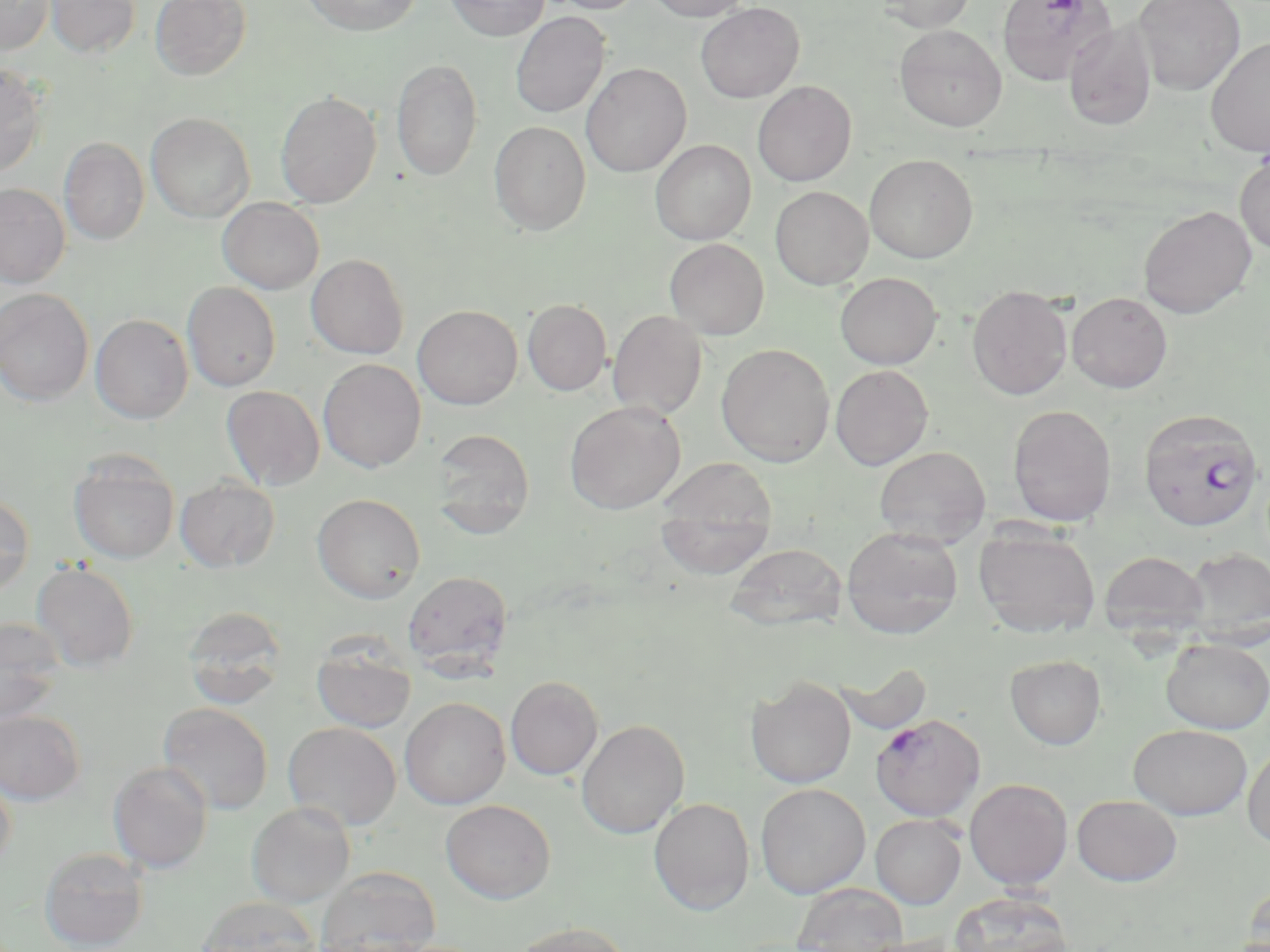

slide-level diagnosis = Plasmodium falciparum
image size = 1270×952 pixels
modality = optical microscopy
stain = May-Grünwald-Giemsa
magnification = 1000x
field of view = one of a larger specimen
preparation = thin blood film
Plasmodium falciparum-infected red blood cell locations = approximate bounding boxes as named x1/y1/x2/y2 corners in pixels: (x1=1138, y1=408, x2=1264, y2=532), (x1=870, y1=713, x2=985, y2=820)
uninfected red blood cell locations = approximate bounding boxes as named x1/y1/x2/y2 corners in pixels: (x1=0, y1=0, x2=54, y2=55), (x1=45, y1=0, x2=141, y2=58), (x1=150, y1=0, x2=252, y2=81), (x1=300, y1=0, x2=422, y2=36), (x1=445, y1=0, x2=548, y2=40), (x1=544, y1=0, x2=646, y2=15), (x1=644, y1=0, x2=754, y2=21), (x1=877, y1=0, x2=976, y2=32), (x1=997, y1=0, x2=1115, y2=86), (x1=1133, y1=0, x2=1246, y2=95), (x1=695, y1=2, x2=804, y2=103), (x1=510, y1=11, x2=610, y2=119), (x1=1064, y1=20, x2=1157, y2=130), (x1=894, y1=25, x2=1007, y2=131), (x1=1205, y1=38, x2=1270, y2=157), (x1=391, y1=58, x2=483, y2=181), (x1=581, y1=63, x2=691, y2=178), (x1=0, y1=64, x2=50, y2=177), (x1=753, y1=81, x2=856, y2=186), (x1=275, y1=91, x2=381, y2=209), (x1=146, y1=112, x2=255, y2=223), (x1=489, y1=121, x2=591, y2=236), (x1=59, y1=138, x2=149, y2=245), (x1=650, y1=139, x2=756, y2=245), (x1=864, y1=154, x2=978, y2=263), (x1=1234, y1=156, x2=1270, y2=255), (x1=0, y1=183, x2=70, y2=287), (x1=770, y1=186, x2=873, y2=289), (x1=217, y1=197, x2=324, y2=294), (x1=1138, y1=205, x2=1257, y2=318), (x1=664, y1=238, x2=769, y2=340), (x1=306, y1=253, x2=409, y2=359), (x1=835, y1=273, x2=942, y2=369), (x1=182, y1=281, x2=281, y2=392), (x1=967, y1=285, x2=1073, y2=400), (x1=0, y1=288, x2=94, y2=406), (x1=1067, y1=292, x2=1173, y2=393), (x1=523, y1=299, x2=612, y2=395), (x1=412, y1=305, x2=523, y2=410), (x1=608, y1=310, x2=708, y2=420), (x1=90, y1=313, x2=193, y2=423), (x1=716, y1=343, x2=835, y2=466), (x1=318, y1=358, x2=426, y2=472), (x1=830, y1=365, x2=933, y2=469), (x1=222, y1=385, x2=326, y2=490), (x1=565, y1=401, x2=685, y2=514), (x1=1007, y1=404, x2=1117, y2=526), (x1=428, y1=428, x2=536, y2=536), (x1=874, y1=446, x2=990, y2=547), (x1=68, y1=452, x2=180, y2=565), (x1=655, y1=460, x2=778, y2=578), (x1=175, y1=477, x2=280, y2=573), (x1=0, y1=492, x2=34, y2=596), (x1=312, y1=493, x2=426, y2=603), (x1=973, y1=525, x2=1101, y2=639), (x1=842, y1=526, x2=964, y2=639), (x1=725, y1=543, x2=846, y2=632), (x1=1180, y1=547, x2=1270, y2=648), (x1=1099, y1=550, x2=1209, y2=640), (x1=31, y1=561, x2=139, y2=672), (x1=402, y1=570, x2=514, y2=673), (x1=182, y1=605, x2=288, y2=710), (x1=0, y1=617, x2=66, y2=722), (x1=1160, y1=638, x2=1269, y2=733), (x1=311, y1=639, x2=417, y2=734), (x1=1005, y1=655, x2=1106, y2=749), (x1=834, y1=660, x2=933, y2=735), (x1=505, y1=676, x2=603, y2=780), (x1=746, y1=676, x2=857, y2=788), (x1=400, y1=697, x2=510, y2=809), (x1=158, y1=702, x2=273, y2=814), (x1=0, y1=710, x2=85, y2=805), (x1=576, y1=720, x2=689, y2=839), (x1=283, y1=721, x2=401, y2=830), (x1=1128, y1=724, x2=1251, y2=819), (x1=1242, y1=742, x2=1270, y2=849), (x1=107, y1=761, x2=213, y2=873), (x1=0, y1=772, x2=16, y2=874), (x1=964, y1=778, x2=1073, y2=890), (x1=755, y1=783, x2=870, y2=898), (x1=1072, y1=795, x2=1182, y2=886), (x1=649, y1=797, x2=755, y2=914), (x1=441, y1=799, x2=556, y2=904), (x1=246, y1=801, x2=355, y2=907), (x1=870, y1=814, x2=966, y2=909), (x1=39, y1=847, x2=149, y2=951), (x1=315, y1=867, x2=441, y2=952), (x1=1241, y1=880, x2=1270, y2=952), (x1=792, y1=882, x2=908, y2=951), (x1=949, y1=891, x2=1073, y2=952), (x1=195, y1=895, x2=323, y2=952), (x1=508, y1=922, x2=634, y2=952), (x1=855, y1=933, x2=964, y2=952)